Outline each Plasmodium vivax-infected red blood cell.
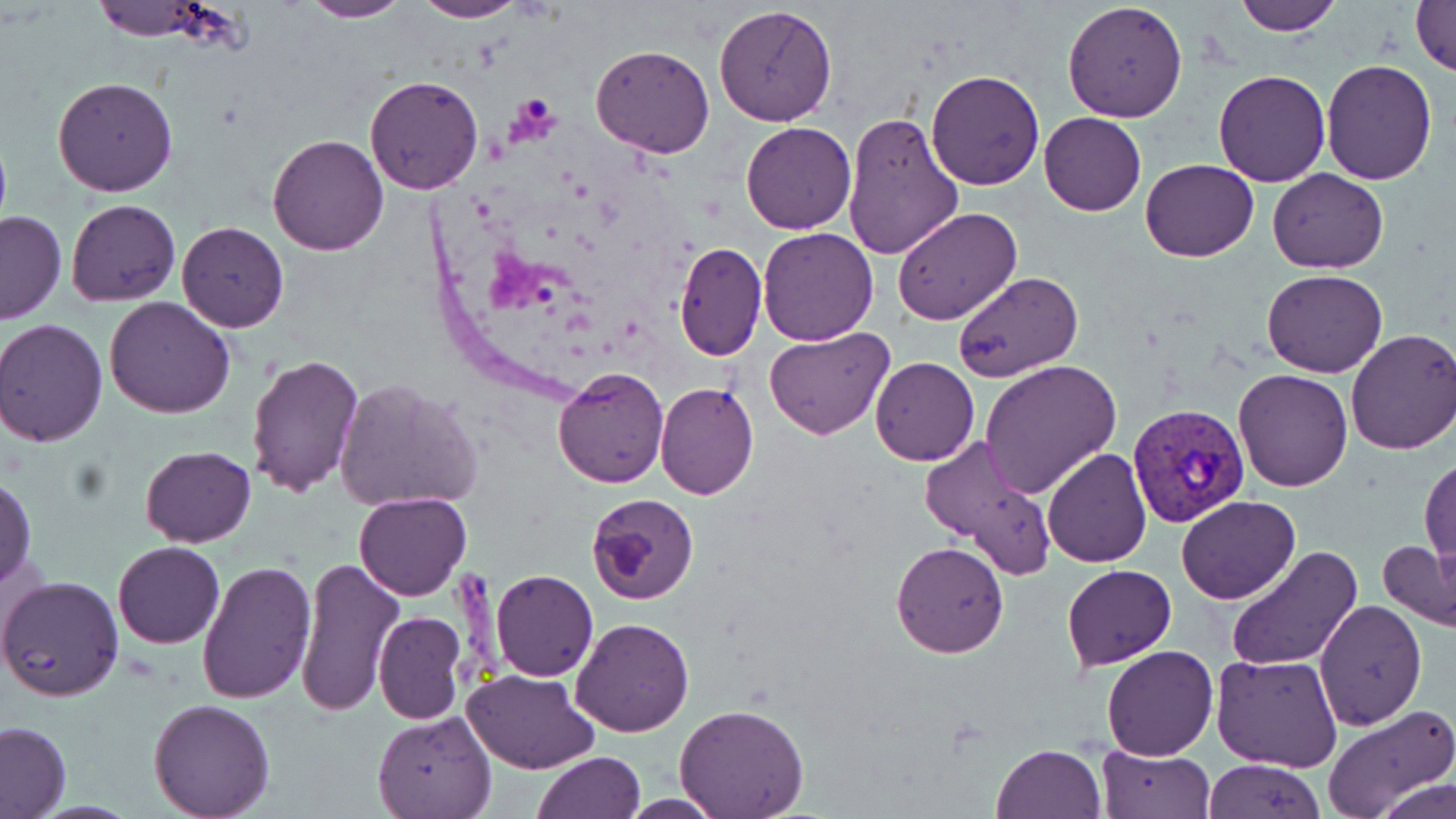
Approximate bounding boxes as (x1,y1)-(x2,y2) corner pairs in pixels.
Plasmodium vivax-infected red blood cells: (1126,404)-(1252,530).

Summary:
  - Uninfected red blood cell locations: (296,0)-(412,23), (410,0)-(531,23), (1232,0)-(1342,35), (1410,0)-(1456,77), (85,1)-(247,47), (1061,1)-(1188,122), (713,4)-(837,126), (590,44)-(714,159), (1319,60)-(1438,185), (927,69)-(1045,190), (1213,69)-(1331,186), (364,74)-(483,195), (53,77)-(178,197), (840,111)-(964,261), (1039,111)-(1146,216), (740,120)-(856,235), (267,133)-(390,255), (1141,158)-(1259,262), (1267,168)-(1388,273), (66,199)-(180,306), (893,207)-(1021,326), (0,210)-(66,325), (175,221)-(289,332), (757,227)-(880,347), (675,241)-(765,360), (1262,269)-(1386,378), (952,271)-(1083,384), (103,297)-(236,420), (4,315)-(216,433), (0,319)-(109,446), (766,326)-(893,440), (1346,328)-(1456,456), (243,350)-(364,498), (869,356)-(979,465), (980,358)-(1121,499), (554,365)-(669,487), (1232,368)-(1353,492), (333,377)-(485,515), (654,382)-(758,499), (918,436)-(1056,578), (138,445)-(256,546), (1043,447)-(1152,567), (1420,455)-(1455,565), (0,474)-(37,586), (354,492)-(471,602), (587,493)-(699,604), (1176,496)-(1301,604), (890,540)-(1009,657), (1378,540)-(1455,633), (112,542)-(224,648), (1226,546)-(1362,672), (296,556)-(403,717), (196,559)-(317,706), (1062,565)-(1177,669), (490,569)-(599,683), (1,575)-(125,702), (1315,599)-(1425,729), (373,611)-(466,723), (570,617)-(694,736), (1100,645)-(1217,761), (1213,654)-(1343,772), (463,668)-(600,775), (147,699)-(276,817), (674,702)-(809,819), (1322,703)-(1455,819), (370,712)-(495,819), (0,721)-(72,819), (994,743)-(1106,819), (1097,746)-(1214,819), (532,751)-(646,819), (1203,758)-(1325,818), (1374,777)-(1454,819), (617,795)-(728,818)
  - Slide-level diagnosis: Plasmodium vivax
  - Modality: light microscopy
  - Field of view: one of a larger specimen
  - Magnification: 1000x
  - Preparation: thin blood smear
  - Stain: May-Grünwald-Giemsa
  - Image size: 1456×819 pixels